Report the malaria status of this cell.
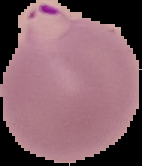

It is parasitized.

Summary:
  - Image size: 142×166 pixels
  - Preparation: thin blood smear
  - Image type: segmented cell region on a black background